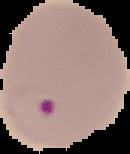
Summary:
  - Image type: segmented cell region on a black background
  - Image size: 130×154 pixels
  - Preparation: thin blood film
  - Result: malaria parasites identified